Comment on the morphology of the red blood cells.
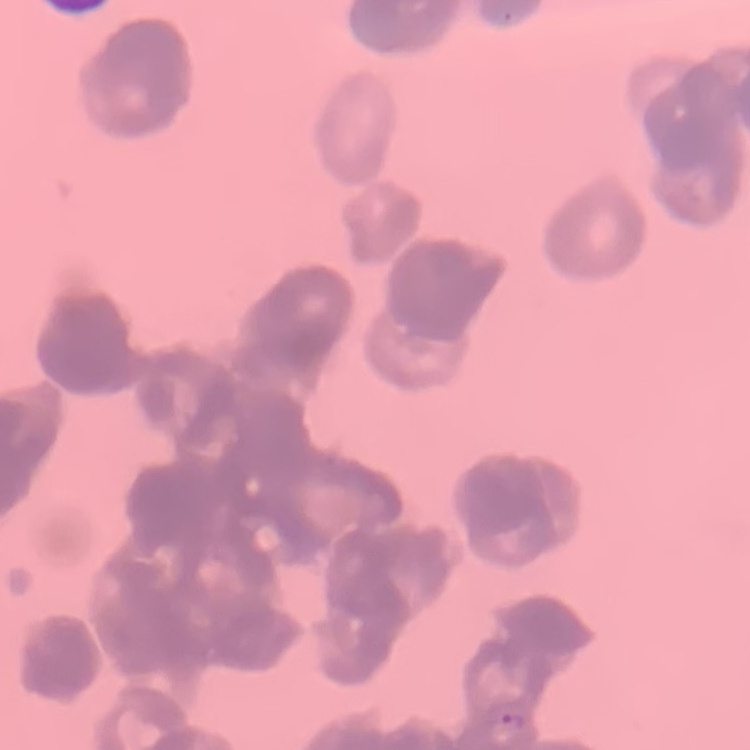
Rouleaux formation.

image_type: one tile cut from a larger photomicrograph
stain: Field's or Giemsa
preparation: thin blood smear